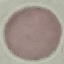

Malaria status: uninfected. Automatically extracted cell patch, resized to 64 × 64 pixels. Thin blood smear. Giemsa stain. Acquired by smartphone through the microscope eyepiece.